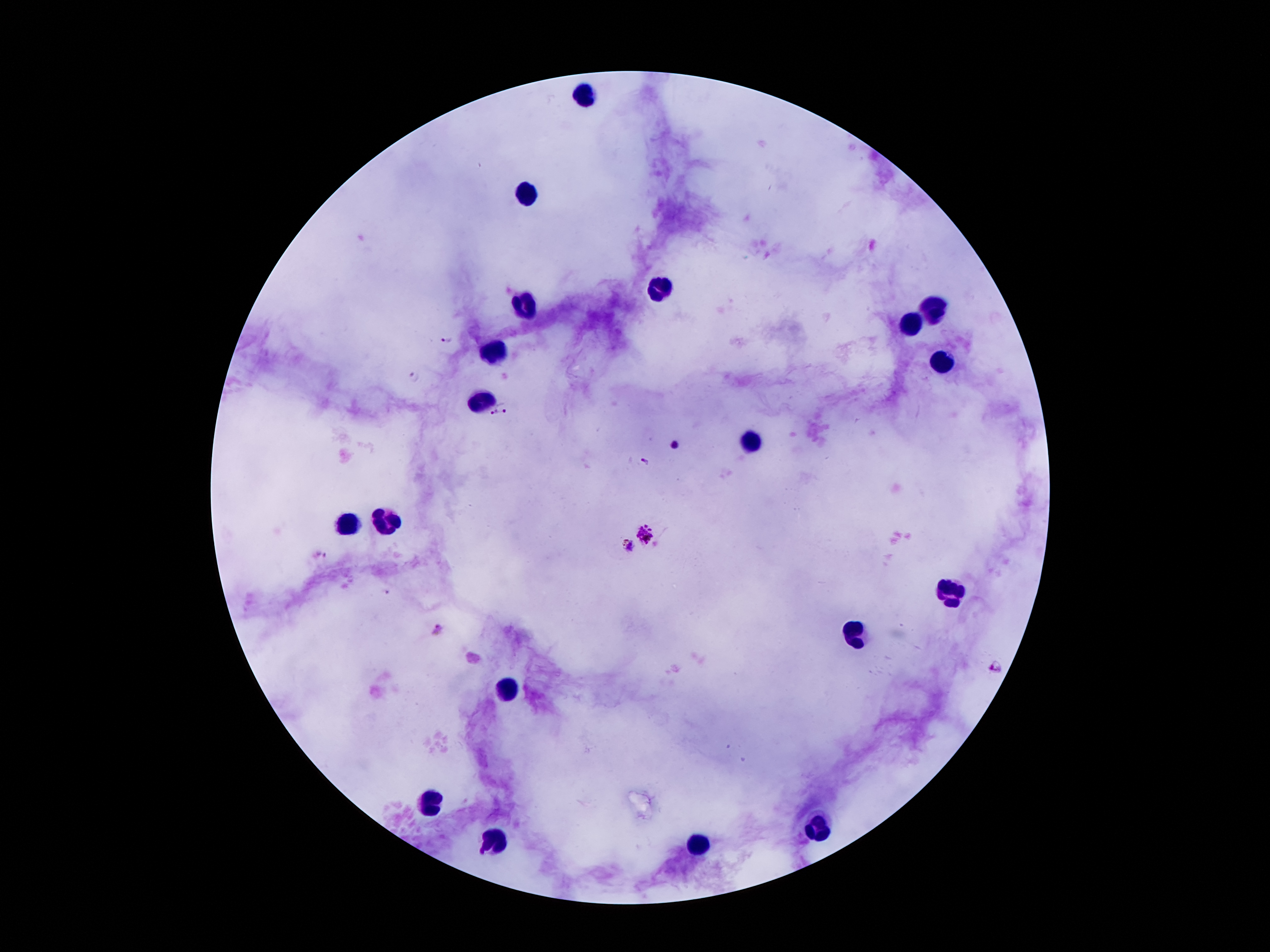 Approximate centers as (x, y) in pixels. Leukocyte locations: (586, 93), (522, 195), (658, 292), (522, 301), (933, 308), (908, 326), (495, 349), (940, 361), (479, 399), (754, 444), (384, 522), (345, 524), (953, 592), (856, 631), (506, 692), (434, 799), (819, 826), (493, 842), (695, 842). Plasmodium parasite locations: (445, 339), (414, 376), (504, 407), (493, 413), (674, 444), (645, 457), (647, 533), (628, 547), (322, 553), (387, 592), (439, 628), (998, 667). 100x magnification. Patient malaria status: positive for Plasmodium falciparum. One field from this slide. Smartphone photograph taken through the microscope eyepiece. Giemsa stain. Thick blood film. Image is 1270×952 pixels.